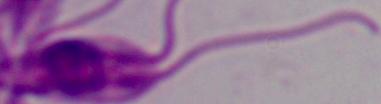

identification = Leishmania
magnification = 1000x
modality = micrograph